Assess this cell for malaria.
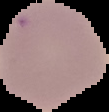

It is uninfected.

image_size: 109×112 pixels
preparation: thin blood film
image_type: segmented cell region with the area outside set to black